Describe the morphology of the red blood cells.
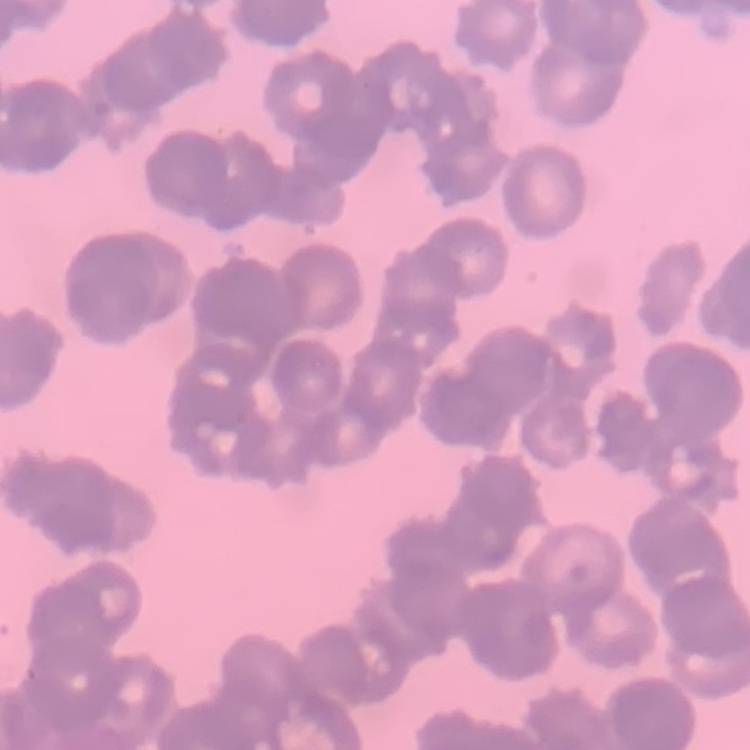
Rouleaux formation.

image_type: square crop of a larger photomicrograph
stain: Field's or Giemsa
preparation: thin peripheral smear